Assess the morphology of the erythrocytes.
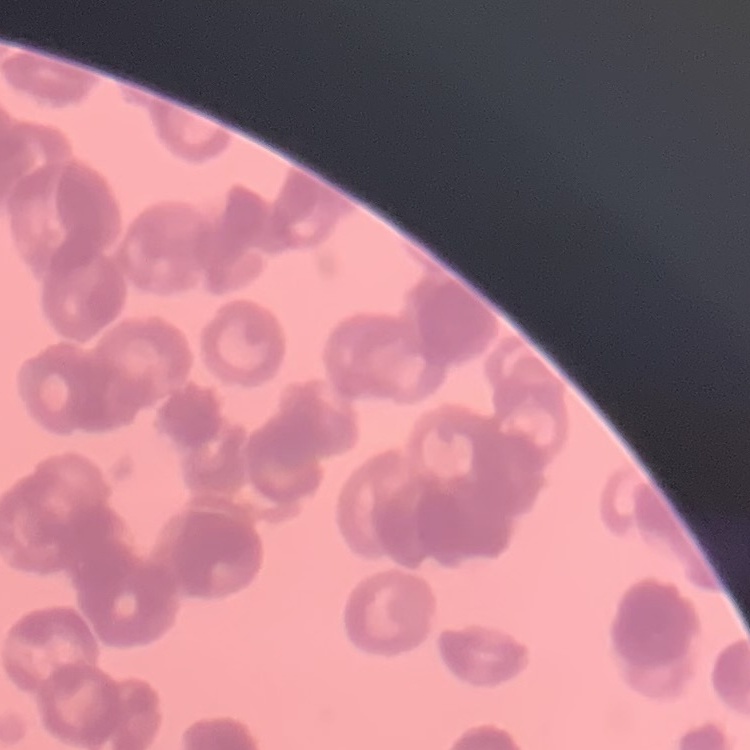

Rouleaux formation.

Thin blood smear. One tile cut from a larger photomicrograph. Field's or Giemsa stain.